State the blood parasite species.
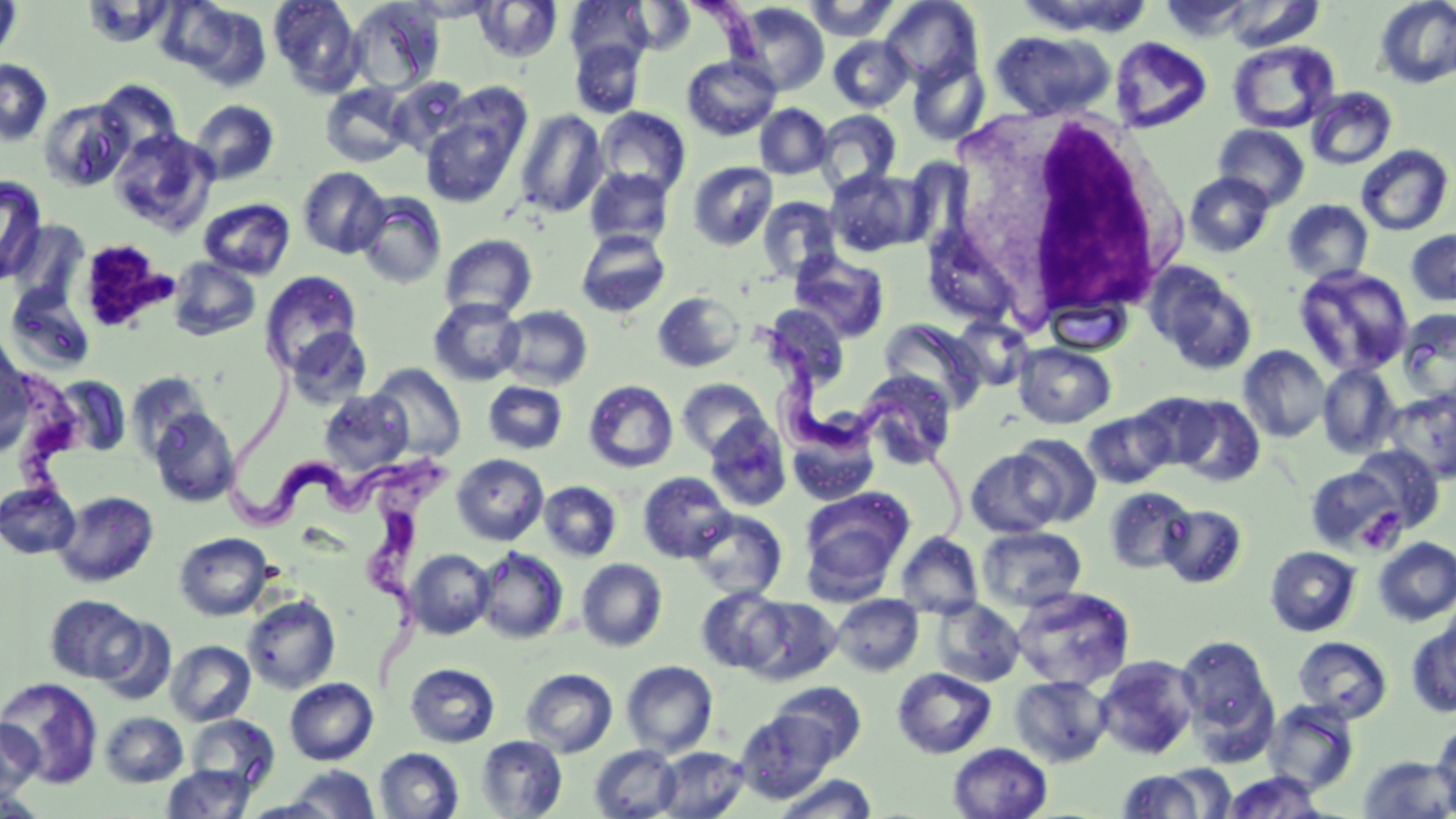

Trypanosoma brucei.

Summary:
  - Coordinate format: approximate bounding boxes as named x1/y1/x2/y2 corners in pixels
  - Trypanosoma brucei locations: (x1=697, y1=2, x2=767, y2=58), (x1=763, y1=330, x2=972, y2=569), (x1=231, y1=368, x2=402, y2=529), (x1=349, y1=459, x2=461, y2=688)
  - White blood cell locations: (x1=935, y1=108, x2=1187, y2=335)
  - Platelet locations: (x1=77, y1=239, x2=176, y2=333), (x1=1356, y1=507, x2=1406, y2=554)
  - Uninfected red blood cell locations: (x1=0, y1=0, x2=23, y2=64), (x1=269, y1=0, x2=364, y2=96), (x1=405, y1=0, x2=499, y2=21), (x1=803, y1=0, x2=900, y2=41), (x1=1374, y1=0, x2=1456, y2=88), (x1=172, y1=1, x2=273, y2=90), (x1=346, y1=1, x2=444, y2=93), (x1=475, y1=1, x2=563, y2=62), (x1=566, y1=1, x2=652, y2=71), (x1=628, y1=1, x2=695, y2=53), (x1=880, y1=1, x2=983, y2=86), (x1=732, y1=2, x2=830, y2=96), (x1=990, y1=30, x2=1115, y2=120), (x1=828, y1=36, x2=913, y2=112), (x1=1110, y1=37, x2=1212, y2=133), (x1=571, y1=40, x2=645, y2=118), (x1=1227, y1=40, x2=1340, y2=134), (x1=682, y1=55, x2=781, y2=140), (x1=908, y1=56, x2=990, y2=145), (x1=0, y1=59, x2=53, y2=146), (x1=388, y1=77, x2=472, y2=157), (x1=95, y1=80, x2=184, y2=161), (x1=320, y1=82, x2=412, y2=167), (x1=1305, y1=87, x2=1397, y2=170), (x1=37, y1=99, x2=133, y2=192), (x1=189, y1=99, x2=279, y2=185), (x1=755, y1=104, x2=832, y2=179), (x1=596, y1=107, x2=691, y2=198), (x1=516, y1=109, x2=607, y2=219), (x1=813, y1=110, x2=902, y2=195), (x1=421, y1=115, x2=520, y2=207), (x1=1213, y1=124, x2=1310, y2=209), (x1=109, y1=128, x2=216, y2=233), (x1=1355, y1=144, x2=1454, y2=236), (x1=688, y1=161, x2=778, y2=250), (x1=298, y1=166, x2=390, y2=259), (x1=584, y1=167, x2=674, y2=251), (x1=825, y1=168, x2=926, y2=257), (x1=1184, y1=171, x2=1275, y2=257), (x1=0, y1=175, x2=48, y2=285), (x1=354, y1=191, x2=447, y2=289), (x1=757, y1=196, x2=842, y2=282), (x1=198, y1=198, x2=296, y2=279), (x1=1283, y1=199, x2=1374, y2=284), (x1=6, y1=220, x2=91, y2=310), (x1=1405, y1=228, x2=1456, y2=307), (x1=576, y1=230, x2=671, y2=317), (x1=439, y1=234, x2=537, y2=320), (x1=789, y1=250, x2=890, y2=343), (x1=168, y1=257, x2=261, y2=340), (x1=1145, y1=262, x2=1258, y2=375), (x1=1294, y1=265, x2=1415, y2=377), (x1=260, y1=270, x2=363, y2=374), (x1=4, y1=285, x2=98, y2=375), (x1=652, y1=291, x2=745, y2=372), (x1=1044, y1=296, x2=1132, y2=356), (x1=429, y1=298, x2=526, y2=386), (x1=762, y1=304, x2=851, y2=388), (x1=497, y1=305, x2=593, y2=390), (x1=1397, y1=307, x2=1456, y2=405), (x1=952, y1=316, x2=1033, y2=392), (x1=878, y1=317, x2=986, y2=414), (x1=287, y1=327, x2=372, y2=408), (x1=0, y1=341, x2=34, y2=454), (x1=1014, y1=343, x2=1116, y2=428), (x1=1238, y1=344, x2=1331, y2=443), (x1=1317, y1=362, x2=1401, y2=458), (x1=369, y1=364, x2=466, y2=460), (x1=856, y1=370, x2=958, y2=469), (x1=126, y1=371, x2=215, y2=461), (x1=49, y1=375, x2=132, y2=458), (x1=677, y1=378, x2=768, y2=458), (x1=483, y1=381, x2=567, y2=455), (x1=584, y1=381, x2=678, y2=473), (x1=1383, y1=389, x2=1456, y2=483), (x1=320, y1=390, x2=413, y2=475), (x1=1132, y1=391, x2=1221, y2=470), (x1=1172, y1=396, x2=1265, y2=487), (x1=147, y1=407, x2=240, y2=508), (x1=1083, y1=410, x2=1174, y2=489), (x1=703, y1=416, x2=792, y2=511), (x1=786, y1=417, x2=881, y2=506), (x1=1010, y1=433, x2=1101, y2=526), (x1=1348, y1=444, x2=1444, y2=532), (x1=965, y1=449, x2=1062, y2=537), (x1=452, y1=453, x2=548, y2=545), (x1=1306, y1=465, x2=1406, y2=554), (x1=638, y1=471, x2=735, y2=562), (x1=0, y1=481, x2=81, y2=559), (x1=539, y1=481, x2=621, y2=561), (x1=1104, y1=486, x2=1195, y2=574), (x1=799, y1=488, x2=913, y2=595), (x1=53, y1=491, x2=159, y2=587), (x1=1159, y1=504, x2=1248, y2=589), (x1=689, y1=509, x2=787, y2=599), (x1=977, y1=525, x2=1087, y2=612), (x1=895, y1=531, x2=983, y2=619), (x1=174, y1=532, x2=273, y2=620), (x1=1373, y1=537, x2=1456, y2=626), (x1=475, y1=546, x2=569, y2=644), (x1=1265, y1=546, x2=1360, y2=636), (x1=406, y1=549, x2=494, y2=639), (x1=576, y1=558, x2=667, y2=651), (x1=1011, y1=586, x2=1135, y2=691), (x1=696, y1=587, x2=788, y2=673), (x1=832, y1=594, x2=924, y2=676), (x1=46, y1=595, x2=146, y2=684), (x1=242, y1=595, x2=341, y2=693), (x1=740, y1=596, x2=842, y2=684), (x1=931, y1=598, x2=1026, y2=687), (x1=96, y1=618, x2=177, y2=706), (x1=1406, y1=619, x2=1456, y2=718), (x1=1176, y1=636, x2=1275, y2=736), (x1=1292, y1=636, x2=1393, y2=722), (x1=166, y1=640, x2=255, y2=725), (x1=1094, y1=654, x2=1200, y2=760), (x1=621, y1=660, x2=717, y2=756), (x1=405, y1=663, x2=500, y2=747), (x1=892, y1=667, x2=997, y2=759), (x1=521, y1=668, x2=618, y2=757), (x1=1009, y1=674, x2=1112, y2=766), (x1=1, y1=677, x2=104, y2=788), (x1=285, y1=677, x2=378, y2=764), (x1=769, y1=682, x2=867, y2=767), (x1=1263, y1=699, x2=1360, y2=794), (x1=735, y1=710, x2=835, y2=801), (x1=100, y1=712, x2=188, y2=787), (x1=186, y1=714, x2=280, y2=793), (x1=0, y1=716, x2=43, y2=802), (x1=1433, y1=719, x2=1456, y2=814), (x1=475, y1=735, x2=567, y2=818), (x1=949, y1=743, x2=1052, y2=819), (x1=589, y1=744, x2=681, y2=818), (x1=655, y1=746, x2=749, y2=818), (x1=375, y1=748, x2=464, y2=819), (x1=1357, y1=755, x2=1456, y2=818), (x1=1156, y1=763, x2=1235, y2=817), (x1=161, y1=764, x2=256, y2=818), (x1=284, y1=765, x2=381, y2=818), (x1=1116, y1=768, x2=1213, y2=817), (x1=1222, y1=770, x2=1327, y2=818), (x1=778, y1=773, x2=878, y2=818)
  - Image size: 1456×819 pixels
  - Preparation: thin blood film
  - Magnification: 1000x
  - Field of view: one of a larger specimen
  - Modality: optical microscopy
  - Stain: May-Grünwald-Giemsa